Name the parasite shown.
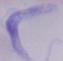
A trypanosome.

Summary:
  - Magnification: 1000x
  - Modality: photomicrograph